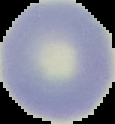
image type = cell region segmented out of the field of view; surrounding area masked to black
image size = 115×124 pixels
result = no Plasmodium parasites seen
preparation = thin blood film